Locate every Plasmodium ovale-infected red blood cell.
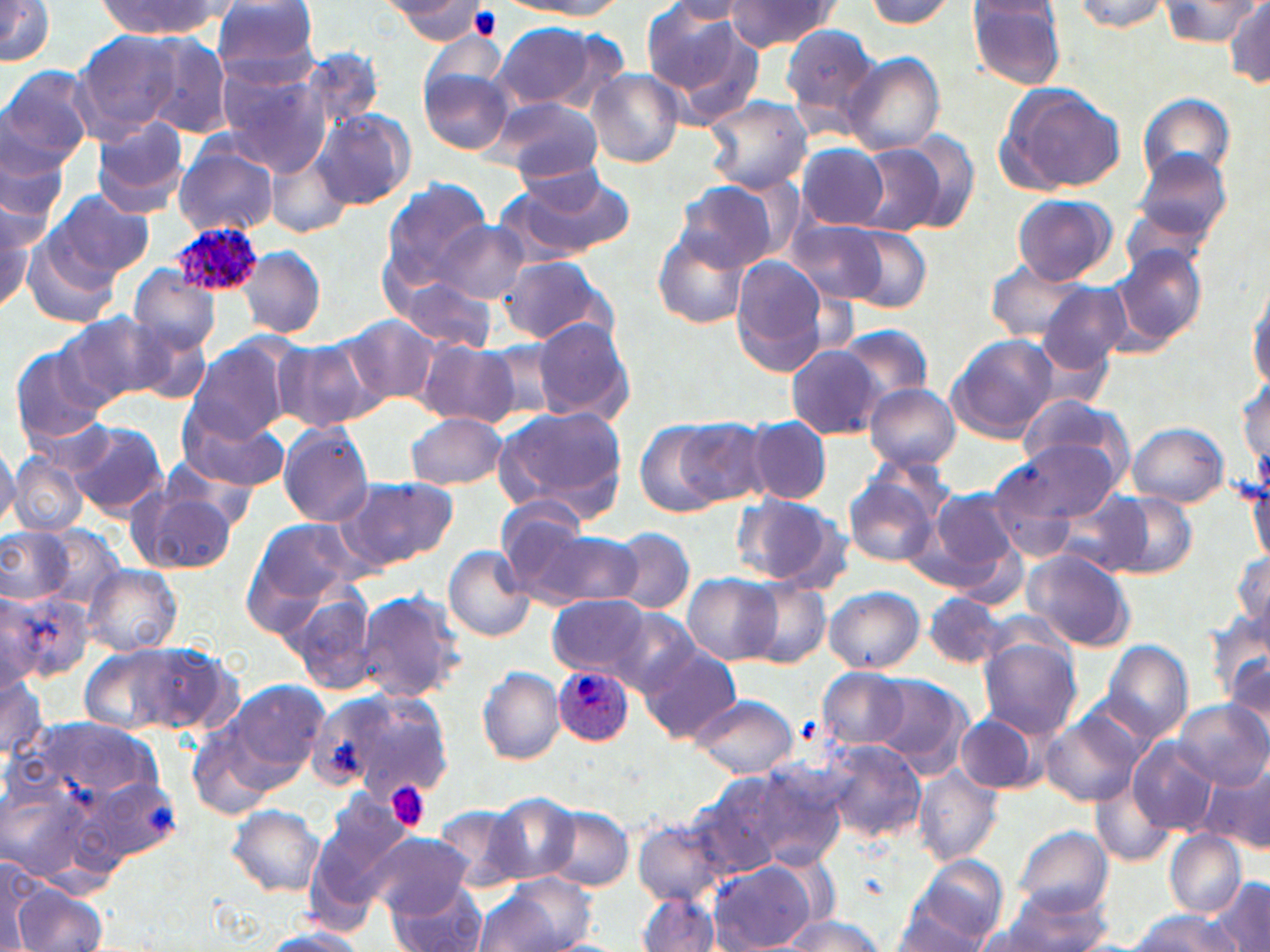

Approximate bounding boxes as (x1, y1, x2, y2) in pixels.
Plasmodium ovale-infected red blood cells: (171, 221, 266, 300), (552, 667, 635, 747).

Summary:
  - Platelet locations: (470, 6, 502, 38), (385, 781, 431, 831)
  - Uninfected red blood cell locations: (376, 0, 478, 21), (508, 0, 626, 18), (723, 0, 839, 54), (859, 0, 959, 31), (1071, 0, 1175, 34), (212, 1, 322, 82), (1156, 1, 1264, 48), (0, 2, 55, 67), (89, 2, 231, 39), (388, 2, 491, 40), (666, 2, 752, 23), (966, 2, 1068, 91), (1225, 2, 1270, 90), (644, 4, 743, 93), (489, 22, 614, 111), (782, 22, 883, 130), (71, 31, 183, 143), (141, 34, 233, 139), (299, 46, 387, 133), (844, 53, 945, 153), (0, 65, 96, 171), (214, 65, 331, 170), (418, 68, 512, 156), (583, 69, 685, 168), (996, 82, 1126, 196), (1137, 92, 1236, 186), (705, 95, 814, 193), (489, 96, 605, 182), (313, 109, 415, 210), (89, 118, 191, 215), (0, 125, 71, 230), (892, 130, 977, 229), (796, 143, 890, 229), (853, 144, 944, 237), (174, 146, 280, 238), (1128, 149, 1235, 255), (269, 153, 352, 239), (497, 168, 636, 263), (380, 179, 494, 286), (674, 185, 778, 273), (46, 190, 155, 282), (1013, 195, 1117, 283), (0, 202, 35, 314), (784, 217, 891, 306), (435, 222, 528, 303), (826, 222, 932, 312), (652, 229, 750, 329), (23, 234, 121, 330), (238, 246, 326, 338), (1112, 246, 1209, 351), (497, 255, 613, 346), (729, 258, 835, 377), (984, 259, 1096, 343), (128, 269, 222, 355), (392, 274, 498, 353), (1248, 278, 1270, 388), (1037, 282, 1132, 373), (59, 312, 173, 407), (337, 313, 441, 409), (532, 317, 635, 425), (123, 319, 215, 403), (835, 325, 935, 403), (946, 334, 1058, 442), (273, 340, 378, 433), (189, 341, 296, 444), (416, 341, 518, 427), (478, 342, 563, 425), (9, 346, 112, 447), (788, 346, 884, 438), (1239, 373, 1268, 476), (865, 383, 960, 470), (1016, 392, 1134, 484), (493, 406, 629, 517), (178, 411, 288, 493), (407, 413, 507, 490), (657, 416, 769, 511), (746, 417, 832, 505), (65, 421, 168, 518), (1128, 422, 1228, 509), (279, 424, 373, 528), (1000, 439, 1123, 525), (0, 441, 20, 536), (8, 455, 85, 537), (1245, 469, 1270, 568), (844, 471, 943, 567), (983, 471, 1085, 563), (340, 477, 457, 570), (128, 485, 237, 574), (925, 490, 1021, 582), (1110, 493, 1198, 578), (731, 494, 844, 589), (1059, 495, 1151, 570), (499, 500, 596, 600), (248, 518, 362, 611), (0, 527, 73, 603), (39, 528, 124, 611), (609, 529, 695, 614), (527, 531, 641, 609), (443, 546, 536, 643), (1025, 550, 1138, 651), (1232, 552, 1269, 629), (84, 565, 183, 656), (683, 572, 781, 664), (746, 582, 830, 669), (823, 586, 926, 673), (284, 589, 378, 695), (356, 590, 467, 703), (2, 593, 91, 686), (924, 594, 1008, 669), (547, 595, 649, 677), (606, 607, 700, 697), (1207, 611, 1270, 708), (978, 638, 1081, 738), (1103, 639, 1194, 740), (81, 641, 229, 738), (638, 646, 741, 746), (1223, 655, 1270, 742), (478, 667, 565, 764), (819, 667, 911, 749), (0, 674, 49, 767), (866, 675, 970, 775), (218, 681, 331, 786), (311, 688, 456, 808), (687, 694, 798, 778), (1174, 700, 1267, 788), (1041, 709, 1147, 808), (955, 714, 1040, 794), (189, 730, 272, 820), (1128, 738, 1219, 836), (824, 742, 927, 842), (712, 760, 851, 876), (1203, 760, 1270, 855), (914, 766, 1003, 865), (692, 773, 793, 873), (1093, 777, 1176, 867), (484, 791, 581, 885), (305, 794, 408, 922), (226, 804, 326, 896), (435, 805, 526, 893), (542, 805, 634, 890), (634, 818, 728, 908), (1014, 825, 1113, 918), (1166, 831, 1246, 917), (365, 832, 473, 916), (904, 857, 1010, 948), (2, 860, 45, 951), (708, 863, 815, 950), (483, 873, 598, 952), (1210, 878, 1269, 951), (12, 880, 107, 952), (390, 886, 487, 952), (637, 892, 721, 951), (991, 892, 1115, 951), (888, 906, 993, 952), (1128, 910, 1242, 951), (779, 914, 885, 951), (255, 927, 371, 952)
  - Slide-level diagnosis: Plasmodium ovale
  - Image size: 1270×952 pixels
  - Magnification: 1000x
  - Field of view: one of a larger specimen
  - Preparation: thin blood film
  - Stain: May-Grünwald-Giemsa
  - Modality: optical microscopy